State the blood parasite species.
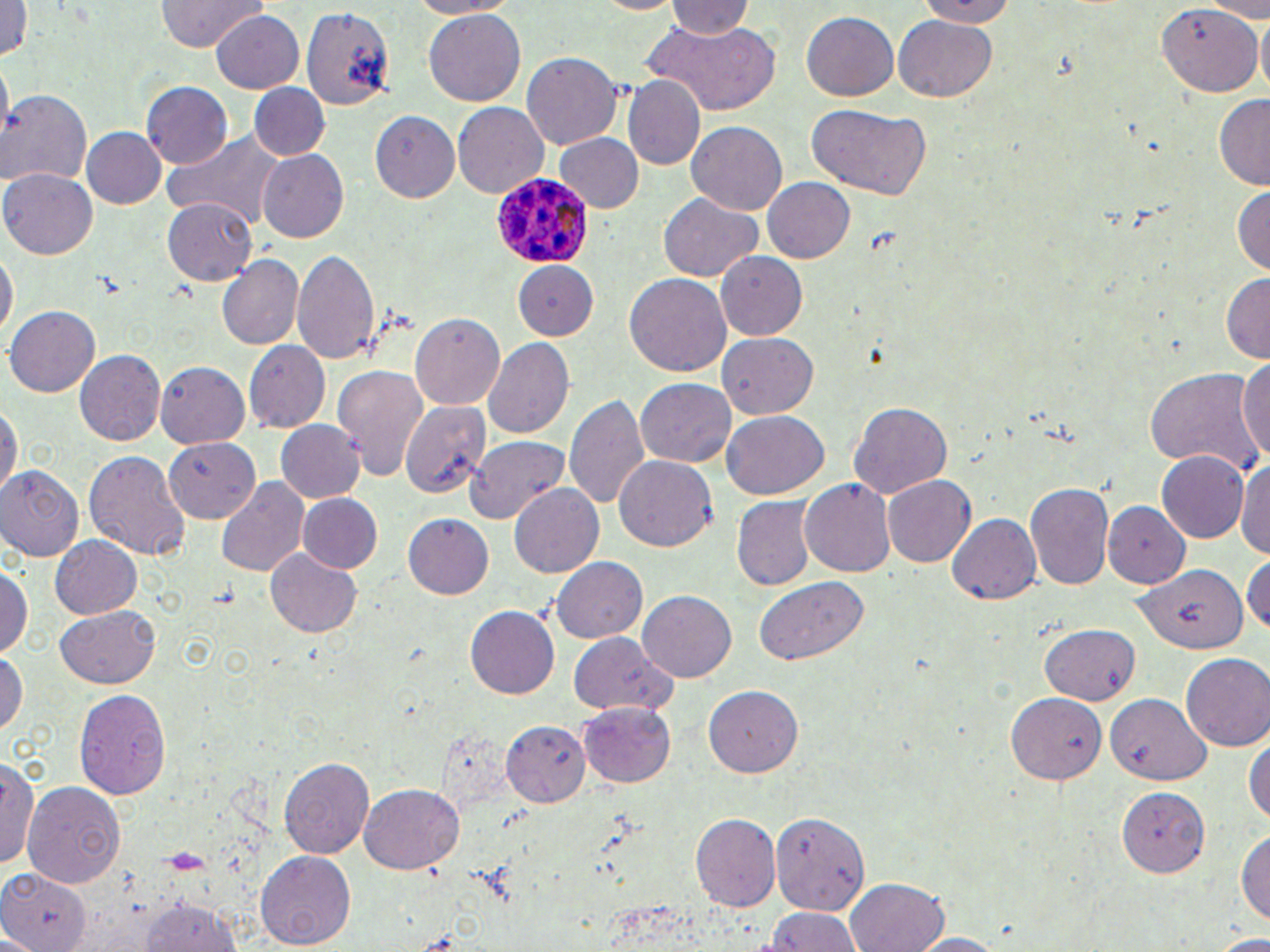
Plasmodium ovale.

Approximate bounding boxes as named x1/y1/x2/y2 corners in pixels. Uninfected red blood cell locations: (x1=154, y1=0, x2=267, y2=53), (x1=409, y1=0, x2=523, y2=17), (x1=911, y1=0, x2=1020, y2=26), (x1=1, y1=1, x2=31, y2=68), (x1=665, y1=1, x2=753, y2=43), (x1=302, y1=5, x2=395, y2=111), (x1=1157, y1=5, x2=1262, y2=98), (x1=209, y1=11, x2=305, y2=93), (x1=422, y1=11, x2=526, y2=106), (x1=800, y1=12, x2=898, y2=101), (x1=1255, y1=14, x2=1269, y2=98), (x1=894, y1=15, x2=996, y2=101), (x1=645, y1=21, x2=782, y2=114), (x1=522, y1=51, x2=621, y2=150), (x1=622, y1=76, x2=705, y2=170), (x1=141, y1=82, x2=230, y2=170), (x1=249, y1=84, x2=330, y2=160), (x1=0, y1=91, x2=92, y2=190), (x1=1214, y1=93, x2=1270, y2=187), (x1=805, y1=102, x2=932, y2=200), (x1=451, y1=103, x2=547, y2=199), (x1=371, y1=111, x2=461, y2=202), (x1=686, y1=123, x2=786, y2=217), (x1=78, y1=127, x2=167, y2=210), (x1=166, y1=129, x2=286, y2=231), (x1=553, y1=134, x2=644, y2=214), (x1=260, y1=149, x2=352, y2=241), (x1=2, y1=167, x2=97, y2=259), (x1=762, y1=175, x2=856, y2=264), (x1=1232, y1=185, x2=1269, y2=277), (x1=659, y1=195, x2=761, y2=281), (x1=162, y1=199, x2=259, y2=286), (x1=0, y1=248, x2=15, y2=346), (x1=292, y1=248, x2=382, y2=362), (x1=716, y1=252, x2=808, y2=341), (x1=217, y1=254, x2=304, y2=349), (x1=508, y1=262, x2=599, y2=340), (x1=1220, y1=271, x2=1270, y2=362), (x1=623, y1=274, x2=730, y2=379), (x1=6, y1=306, x2=100, y2=396), (x1=409, y1=315, x2=504, y2=411), (x1=718, y1=332, x2=817, y2=419), (x1=484, y1=339, x2=575, y2=439), (x1=244, y1=342, x2=329, y2=432), (x1=74, y1=349, x2=165, y2=446), (x1=1236, y1=352, x2=1270, y2=467), (x1=156, y1=361, x2=251, y2=449), (x1=332, y1=363, x2=431, y2=481), (x1=1145, y1=365, x2=1264, y2=478), (x1=637, y1=379, x2=736, y2=469), (x1=566, y1=391, x2=652, y2=513), (x1=0, y1=400, x2=19, y2=506), (x1=403, y1=401, x2=490, y2=500), (x1=850, y1=402, x2=953, y2=498), (x1=720, y1=413, x2=827, y2=500), (x1=276, y1=421, x2=364, y2=502), (x1=467, y1=435, x2=572, y2=523), (x1=163, y1=437, x2=259, y2=520), (x1=83, y1=450, x2=189, y2=561), (x1=1154, y1=450, x2=1248, y2=542), (x1=613, y1=454, x2=717, y2=551), (x1=1238, y1=454, x2=1270, y2=561), (x1=0, y1=466, x2=85, y2=561), (x1=882, y1=475, x2=976, y2=568), (x1=217, y1=478, x2=309, y2=578), (x1=801, y1=478, x2=894, y2=578), (x1=509, y1=482, x2=603, y2=580), (x1=1025, y1=482, x2=1115, y2=595), (x1=296, y1=493, x2=383, y2=574), (x1=731, y1=499, x2=814, y2=593), (x1=1106, y1=503, x2=1190, y2=590), (x1=946, y1=511, x2=1041, y2=604), (x1=403, y1=516, x2=493, y2=599), (x1=48, y1=534, x2=142, y2=621), (x1=266, y1=550, x2=362, y2=637), (x1=1243, y1=552, x2=1270, y2=636), (x1=550, y1=556, x2=646, y2=644), (x1=1, y1=564, x2=29, y2=660), (x1=1133, y1=566, x2=1246, y2=655), (x1=753, y1=576, x2=872, y2=666), (x1=639, y1=590, x2=737, y2=680), (x1=54, y1=606, x2=160, y2=689), (x1=465, y1=606, x2=560, y2=699), (x1=1040, y1=623, x2=1142, y2=706), (x1=567, y1=633, x2=675, y2=718), (x1=0, y1=650, x2=26, y2=742), (x1=1182, y1=654, x2=1270, y2=751), (x1=704, y1=685, x2=804, y2=776), (x1=74, y1=688, x2=171, y2=801), (x1=1006, y1=695, x2=1104, y2=786), (x1=1106, y1=695, x2=1210, y2=782), (x1=578, y1=702, x2=676, y2=787), (x1=499, y1=715, x2=592, y2=811), (x1=1245, y1=731, x2=1270, y2=826), (x1=2, y1=754, x2=39, y2=874), (x1=277, y1=756, x2=374, y2=859), (x1=358, y1=781, x2=466, y2=873), (x1=24, y1=783, x2=124, y2=891), (x1=1118, y1=787, x2=1211, y2=877), (x1=770, y1=808, x2=874, y2=911), (x1=691, y1=813, x2=780, y2=912), (x1=1237, y1=824, x2=1270, y2=926), (x1=258, y1=851, x2=354, y2=949), (x1=0, y1=866, x2=91, y2=952), (x1=847, y1=878, x2=948, y2=952), (x1=135, y1=896, x2=244, y2=951), (x1=761, y1=905, x2=862, y2=952), (x1=903, y1=932, x2=1012, y2=951). Plasmodium ovale-infected red blood cell locations: (x1=488, y1=170, x2=591, y2=272). Image is 1270×952 pixels. One field of a larger specimen. 1000x magnification. May-Grünwald-Giemsa stain. Thin blood smear. Optical microscopy.